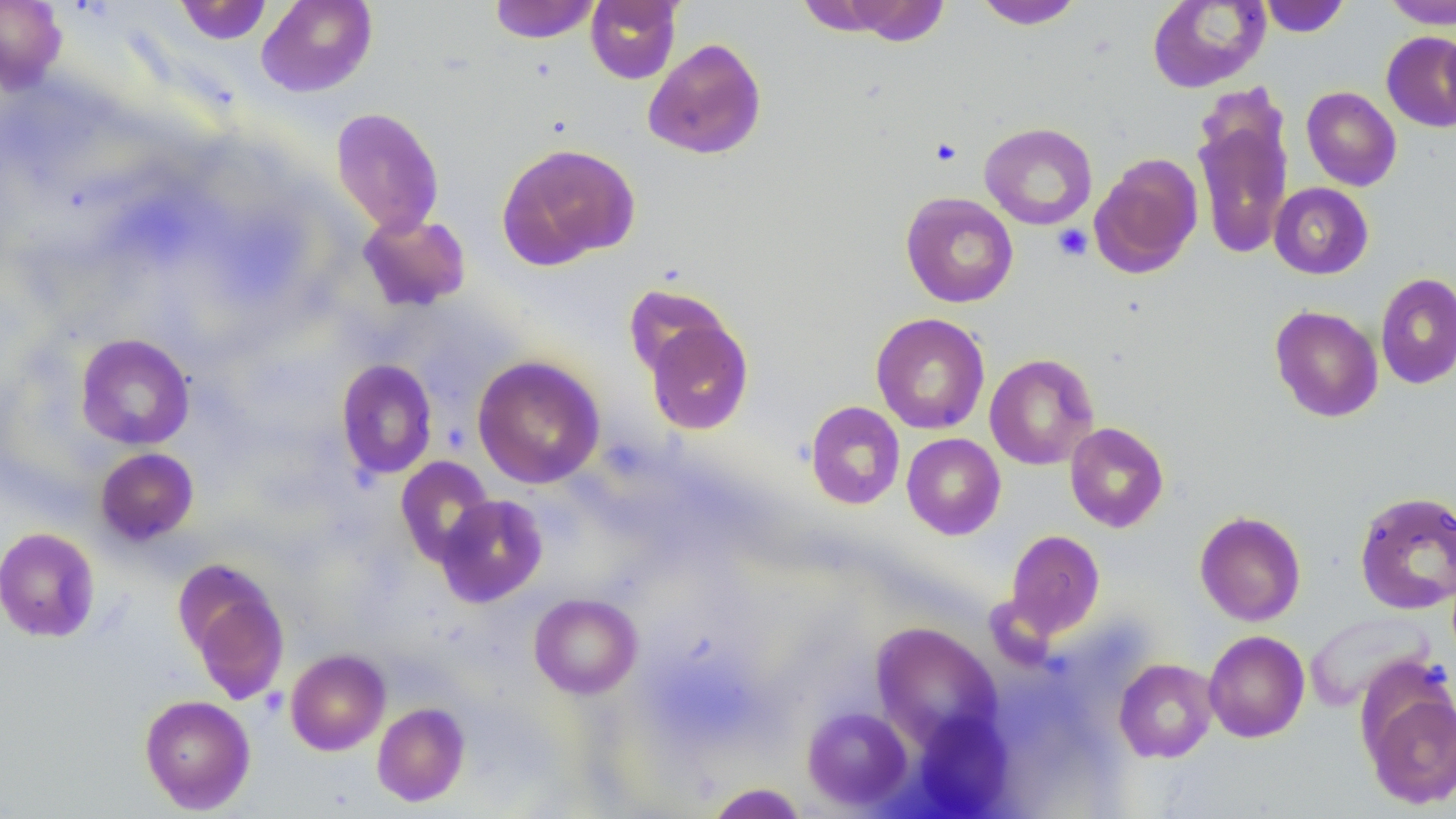

{
  "slide_level_diagnosis": "no evidence of blood parasites",
  "magnification": "1000x",
  "field_of_view": "single",
  "image_size": "1456×819 pixels",
  "platelet_locations": "approximate bounding boxes as named x1/y1/x2/y2 corners in pixels: (x1=930, y1=138, x2=963, y2=166), (x1=1053, y1=224, x2=1093, y2=261)",
  "modality": "light microscopy",
  "preparation": "thin blood film",
  "stain": "May-Grünwald-Giemsa",
  "uninfected_red_blood_cell_locations": "approximate bounding boxes as named x1/y1/x2/y2 corners in pixels: (x1=0, y1=0, x2=67, y2=92), (x1=255, y1=0, x2=378, y2=97), (x1=488, y1=0, x2=601, y2=44), (x1=585, y1=0, x2=682, y2=84), (x1=794, y1=0, x2=912, y2=38), (x1=973, y1=0, x2=1085, y2=29), (x1=1258, y1=0, x2=1351, y2=37), (x1=1382, y1=0, x2=1456, y2=29), (x1=842, y1=1, x2=950, y2=46), (x1=1147, y1=1, x2=1270, y2=93), (x1=1440, y1=25, x2=1456, y2=126), (x1=1381, y1=31, x2=1456, y2=132), (x1=643, y1=38, x2=767, y2=160), (x1=1301, y1=86, x2=1401, y2=191), (x1=1193, y1=106, x2=1293, y2=261), (x1=330, y1=107, x2=445, y2=236), (x1=979, y1=122, x2=1097, y2=230), (x1=496, y1=142, x2=639, y2=269), (x1=1089, y1=153, x2=1203, y2=279), (x1=1269, y1=183, x2=1374, y2=279), (x1=901, y1=192, x2=1018, y2=307), (x1=358, y1=211, x2=472, y2=311), (x1=1375, y1=273, x2=1456, y2=389), (x1=623, y1=284, x2=733, y2=382), (x1=1269, y1=304, x2=1384, y2=423), (x1=871, y1=312, x2=990, y2=435), (x1=642, y1=314, x2=754, y2=435), (x1=75, y1=334, x2=195, y2=450), (x1=984, y1=353, x2=1098, y2=470), (x1=472, y1=355, x2=605, y2=489), (x1=336, y1=359, x2=438, y2=481), (x1=805, y1=401, x2=906, y2=510), (x1=1065, y1=422, x2=1169, y2=532), (x1=902, y1=433, x2=1005, y2=539), (x1=95, y1=447, x2=199, y2=545), (x1=395, y1=456, x2=496, y2=567), (x1=1354, y1=491, x2=1456, y2=614), (x1=435, y1=493, x2=548, y2=607), (x1=1195, y1=511, x2=1306, y2=626), (x1=0, y1=527, x2=100, y2=643), (x1=1005, y1=530, x2=1105, y2=639), (x1=175, y1=561, x2=291, y2=704), (x1=529, y1=593, x2=642, y2=698), (x1=1304, y1=611, x2=1435, y2=710), (x1=871, y1=623, x2=1002, y2=751), (x1=1203, y1=630, x2=1310, y2=743), (x1=285, y1=649, x2=390, y2=755), (x1=1114, y1=658, x2=1217, y2=763), (x1=1362, y1=684, x2=1456, y2=810), (x1=139, y1=694, x2=256, y2=814), (x1=372, y1=702, x2=470, y2=807), (x1=803, y1=706, x2=914, y2=811), (x1=913, y1=711, x2=1013, y2=816), (x1=707, y1=782, x2=806, y2=818)"
}